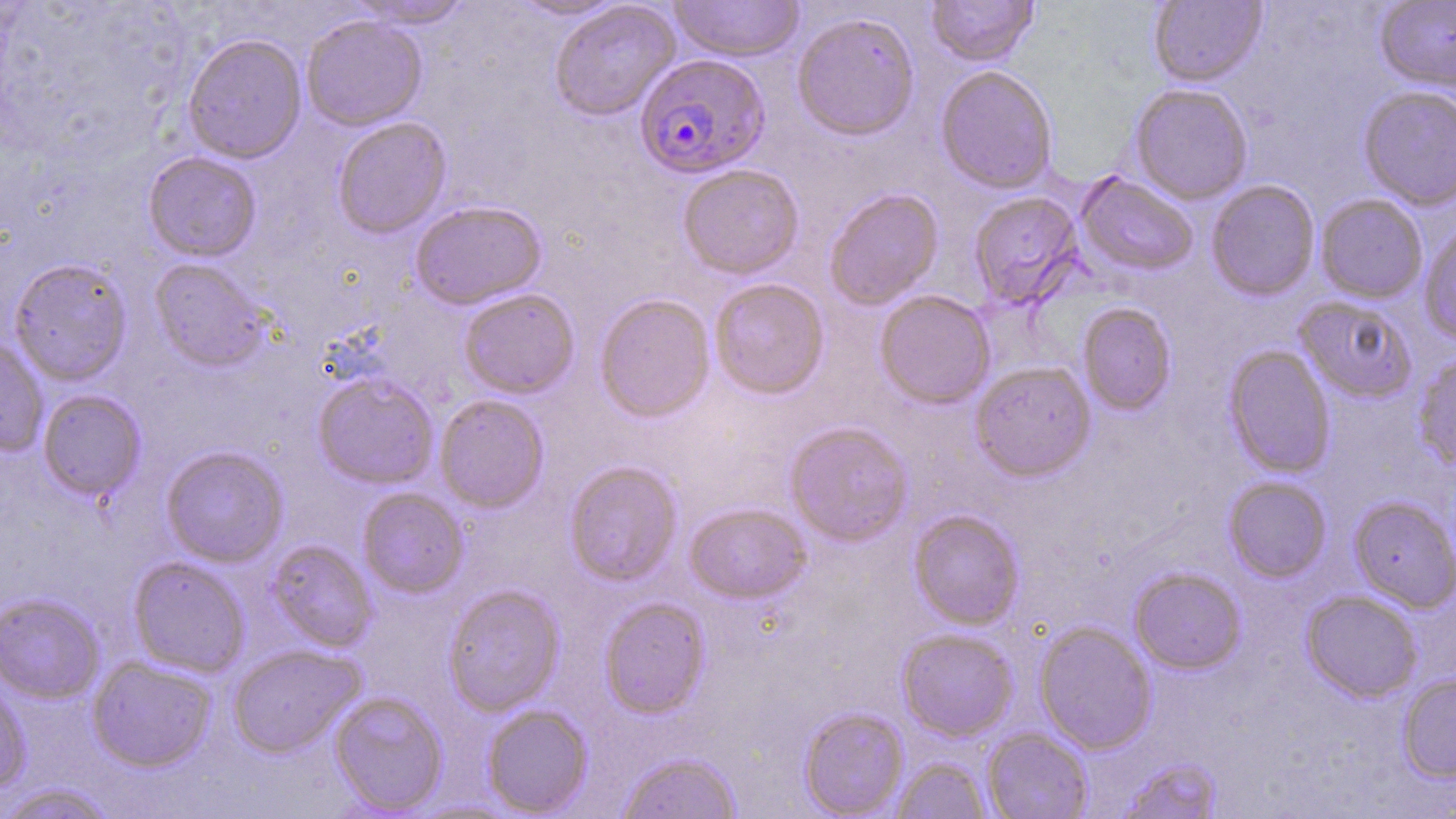 Approximate bounding boxes as (x1, y1, x2, y2) in pixels. Plasmodium falciparum-infected red blood cell locations: (634, 54, 769, 179). Uninfected red blood cell locations: (346, 0, 475, 29), (508, 0, 629, 21), (669, 0, 805, 63), (926, 0, 1038, 67), (548, 1, 681, 121), (1148, 1, 1267, 88), (1374, 1, 1456, 95), (792, 11, 920, 142), (301, 14, 427, 131), (182, 33, 307, 163), (935, 66, 1058, 194), (1130, 84, 1253, 204), (1358, 86, 1456, 211), (332, 117, 452, 239), (143, 152, 261, 262), (678, 165, 804, 279), (1075, 172, 1198, 277), (1206, 181, 1320, 301), (824, 189, 944, 310), (968, 192, 1084, 310), (1315, 195, 1428, 303), (410, 200, 547, 310), (1418, 222, 1456, 346), (8, 258, 132, 386), (149, 258, 270, 372), (709, 278, 829, 399), (458, 288, 580, 399), (874, 290, 996, 410), (595, 294, 715, 422), (1294, 296, 1417, 402), (1078, 303, 1177, 416), (0, 336, 49, 458), (1223, 345, 1336, 479), (1413, 352, 1456, 473), (970, 362, 1096, 482), (313, 374, 439, 489), (37, 390, 146, 502), (435, 395, 549, 513), (785, 422, 913, 546), (161, 446, 288, 567), (564, 461, 683, 587), (1223, 477, 1332, 583), (357, 489, 468, 598), (1349, 496, 1456, 612), (684, 503, 811, 604), (909, 510, 1024, 630), (250, 539, 372, 755), (265, 540, 378, 652), (127, 557, 249, 677), (1130, 568, 1246, 674), (442, 585, 565, 717), (1301, 590, 1422, 703), (0, 593, 105, 704), (599, 597, 710, 718), (1034, 622, 1157, 755), (897, 629, 1018, 742), (227, 644, 366, 758), (86, 656, 217, 772), (1397, 674, 1456, 782), (0, 676, 32, 795), (329, 691, 449, 815), (482, 704, 593, 817), (798, 706, 909, 818), (982, 727, 1093, 818), (618, 751, 742, 819), (891, 757, 991, 819), (1117, 758, 1225, 819), (0, 783, 119, 819). Slide-level diagnosis: Plasmodium falciparum. Image is 1456×819 pixels. May-Grünwald-Giemsa stain. Thin blood smear. 1000x magnification. One field of a larger specimen. Light microscopy.